Assess the morphology of the red blood cells.
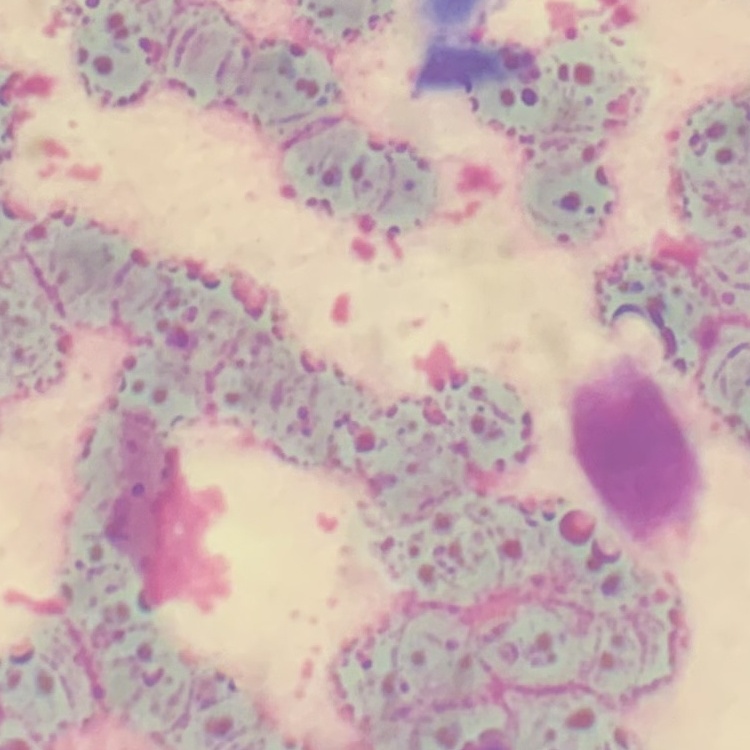

They show rouleaux formation.

Summary:
  - Stain: Field's or Giemsa
  - Image type: one tile cut from a larger photomicrograph
  - Preparation: thin peripheral smear